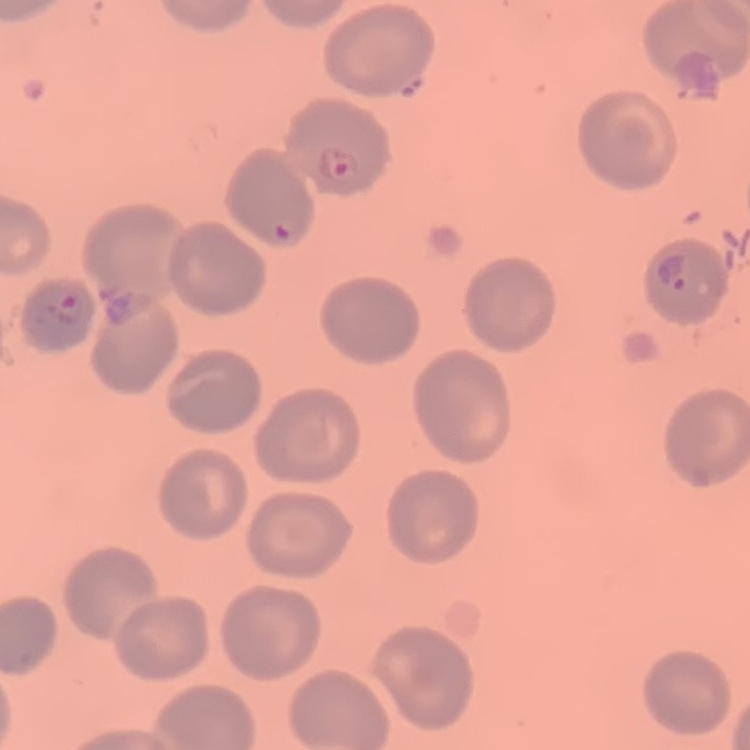
The red blood cells exhibit no rouleaux formation. Field's or Giemsa stain. Thin peripheral smear. One tile cut from a larger photomicrograph.